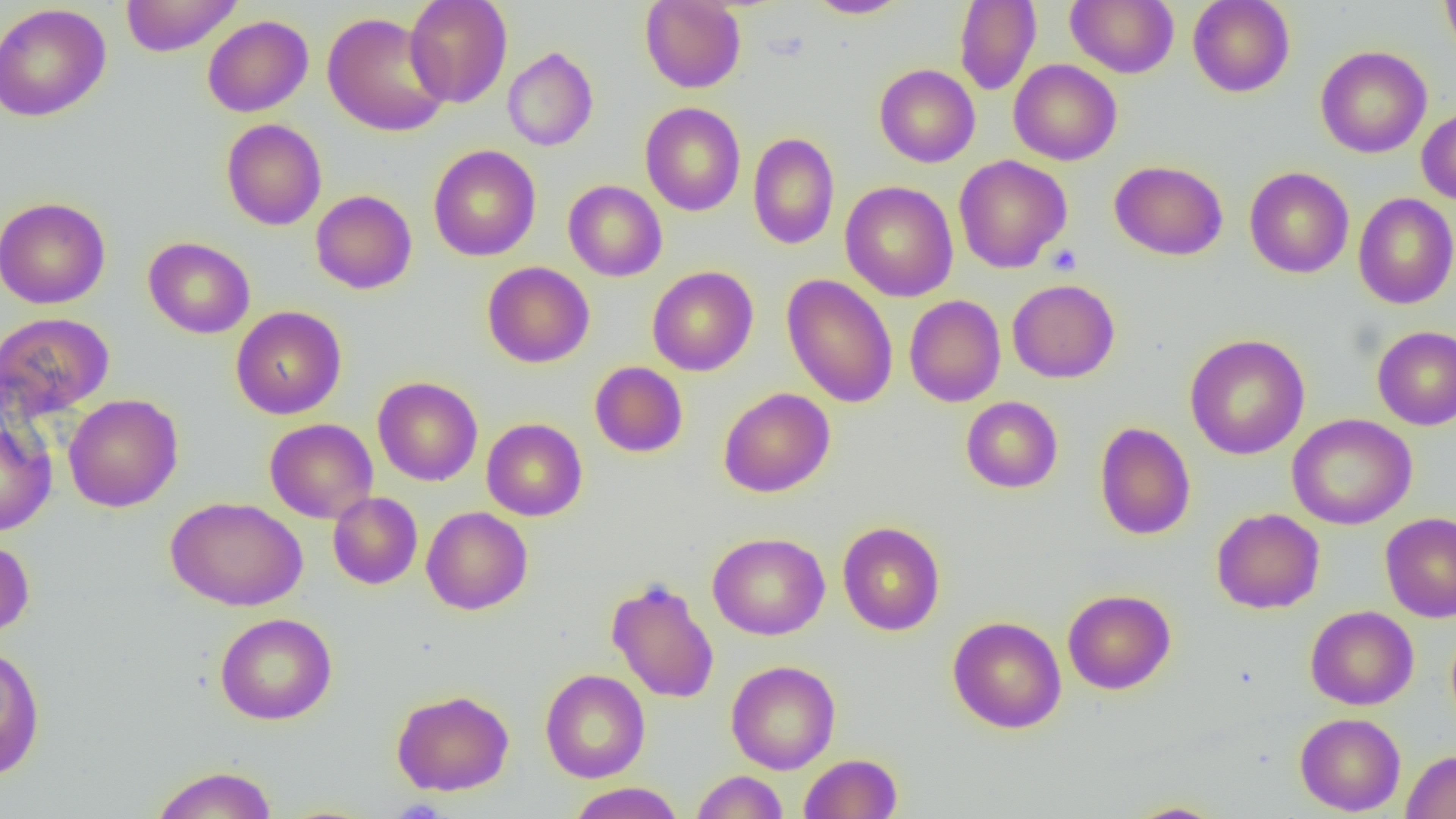
{
  "slide_level_diagnosis": "negative for blood parasites",
  "modality": "optical microscopy",
  "image_size": "1456×819 pixels",
  "magnification": "1000x",
  "field_of_view": "one of a larger specimen",
  "preparation": "thin blood film",
  "uninfected_red_blood_cell_locations": "approximate bounding boxes as [x1, y1, x2, y2] in pixels: [121, 0, 241, 57], [404, 0, 513, 108], [805, 0, 912, 18], [954, 0, 1041, 95], [1066, 0, 1178, 78], [1188, 0, 1295, 97], [1440, 0, 1456, 63], [640, 1, 746, 92], [0, 3, 111, 122], [322, 12, 450, 137], [202, 15, 313, 117], [1315, 45, 1432, 158], [503, 47, 598, 151], [1009, 59, 1122, 165], [874, 64, 980, 167], [639, 102, 746, 216], [1416, 106, 1456, 205], [221, 118, 327, 230], [748, 132, 839, 249], [429, 144, 541, 261], [954, 155, 1071, 273], [1109, 160, 1228, 260], [1244, 166, 1354, 278], [563, 180, 667, 281], [841, 181, 958, 302], [310, 190, 417, 294], [1353, 193, 1456, 309], [0, 196, 111, 309], [143, 236, 255, 338], [482, 261, 595, 367], [647, 266, 758, 376], [781, 274, 898, 408], [1007, 279, 1120, 383], [904, 295, 1006, 407], [231, 305, 346, 419], [0, 311, 114, 420], [1372, 326, 1456, 430], [1185, 333, 1310, 459], [589, 361, 688, 457], [373, 376, 483, 486], [719, 387, 835, 497], [64, 394, 183, 512], [961, 396, 1063, 493], [1287, 413, 1416, 529], [0, 417, 56, 536], [265, 418, 378, 523], [482, 418, 587, 521], [1094, 422, 1196, 540], [328, 492, 423, 589], [166, 496, 307, 611], [421, 507, 533, 615], [1211, 508, 1325, 613], [1380, 512, 1456, 623], [837, 521, 945, 635], [707, 532, 830, 640], [0, 537, 35, 637], [606, 577, 719, 704], [1063, 589, 1176, 694], [1305, 605, 1418, 710], [215, 612, 337, 724], [948, 616, 1066, 733], [0, 644, 45, 780], [726, 660, 840, 774], [540, 668, 650, 783], [391, 688, 514, 796], [1295, 712, 1406, 816], [1402, 750, 1456, 818], [799, 753, 903, 818], [149, 765, 278, 819], [691, 770, 788, 819], [567, 782, 685, 818], [1123, 801, 1228, 818]",
  "platelet_locations": "approximate bounding boxes as [x1, y1, x2, y2] in pixels: [1046, 243, 1082, 275]"
}